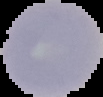 From a thin blood smear. Image is 103×97 pixels. Malaria status: uninfected. Segmented cell region on a black background.